Outline each blood parasite and name the species.
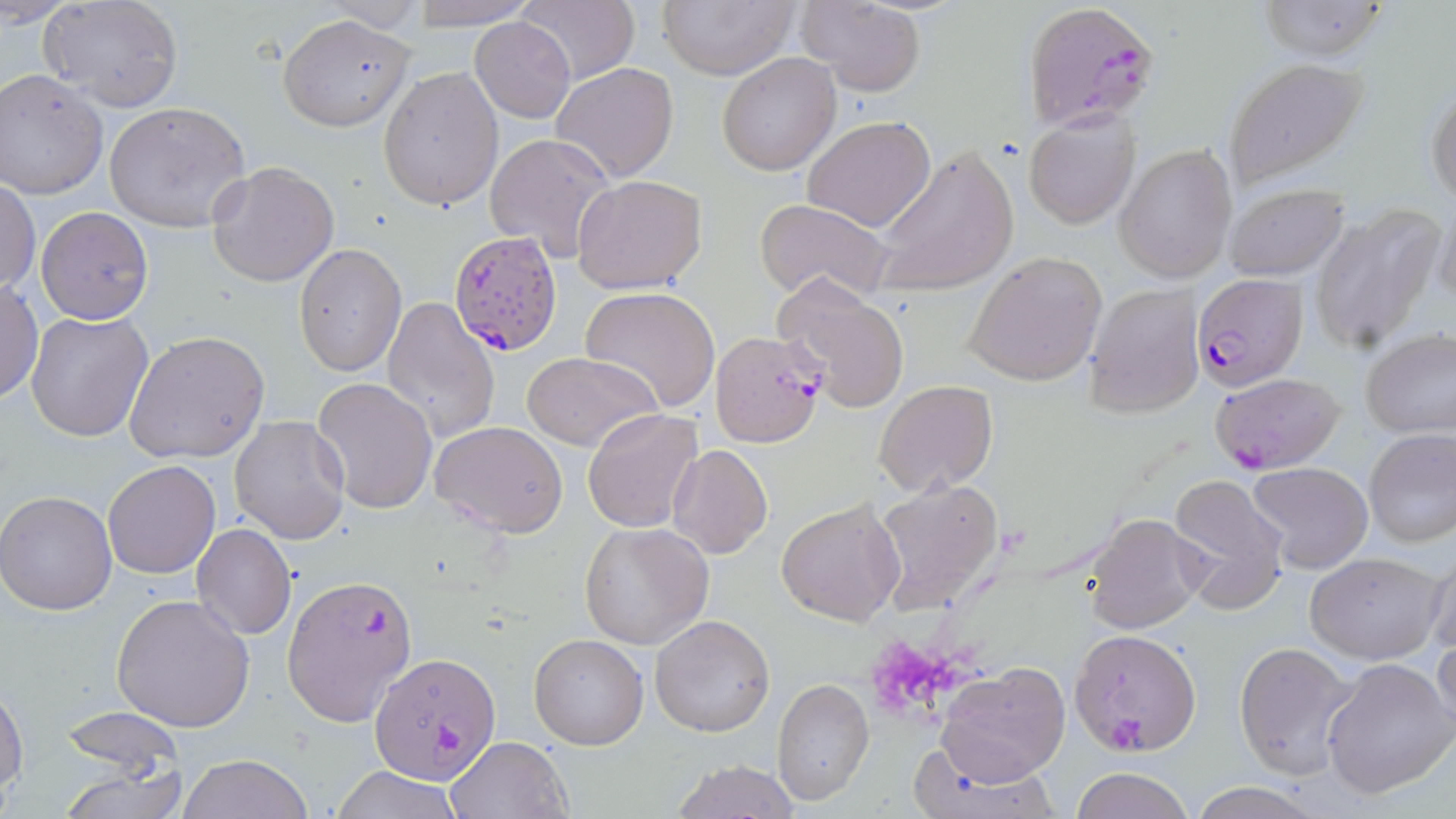

Approximate bounding boxes as (x1,y1)-(x2,y2) corner pairs in pixels.
Plasmodium falciparum-infected red blood cells: (1025,5)-(1161,138), (447,230)-(563,358), (1193,272)-(1307,390), (710,328)-(828,450), (1208,372)-(1347,475), (283,572)-(417,727), (1070,629)-(1202,754), (368,653)-(501,787).
No Plasmodium ovale, Plasmodium malariae, Plasmodium vivax, Babesia divergens, or Trypanosoma brucei observed.

Summary:
  - Uninfected red blood cell locations: (38,0)-(184,111), (405,0)-(534,27), (513,0)-(639,86), (657,0)-(802,79), (799,0)-(926,96), (1258,0)-(1392,61), (319,1)-(427,32), (279,14)-(415,132), (471,15)-(575,122), (716,54)-(840,175), (1224,57)-(1370,188), (550,62)-(679,183), (378,67)-(503,211), (0,70)-(108,200), (1427,85)-(1456,203), (104,100)-(253,233), (1023,110)-(1140,229), (802,116)-(935,234), (485,132)-(617,262), (870,144)-(1019,296), (1114,144)-(1236,283), (207,162)-(339,287), (574,174)-(709,293), (1,180)-(39,294), (1225,182)-(1350,281), (754,198)-(895,305), (1432,203)-(1456,309), (1308,204)-(1444,355), (37,206)-(153,324), (295,243)-(406,377), (963,252)-(1108,387), (773,276)-(910,414), (1,279)-(43,403), (1082,284)-(1203,419), (580,286)-(721,412), (382,297)-(502,443), (26,311)-(153,442), (1359,327)-(1456,439), (124,330)-(270,466), (522,351)-(660,451), (310,375)-(438,514), (875,379)-(999,495), (583,407)-(702,532), (229,414)-(351,545), (430,420)-(570,536), (1364,430)-(1456,548), (666,444)-(773,561), (103,460)-(219,578), (1246,461)-(1374,575), (1166,472)-(1289,615), (872,478)-(1005,612), (0,490)-(117,615), (776,498)-(904,627), (1085,513)-(1207,637), (578,522)-(715,649), (191,523)-(297,640), (1424,545)-(1456,665), (1304,550)-(1445,664), (110,593)-(257,733), (649,613)-(777,738), (1433,633)-(1456,743), (528,634)-(648,750), (1233,641)-(1364,780), (1321,657)-(1456,799), (939,661)-(1070,785), (773,678)-(874,805), (0,683)-(26,802), (59,705)-(184,781), (447,735)-(571,819), (902,741)-(1062,818), (177,754)-(315,819), (668,759)-(802,818), (58,762)-(188,819), (330,766)-(463,819), (1070,766)-(1193,819), (1185,783)-(1326,818)
  - Slide-level diagnosis: Plasmodium falciparum
  - Image size: 1456×819 pixels
  - Magnification: 1000x
  - Modality: light microscopy
  - Field of view: one of a larger specimen
  - Preparation: thin blood film
  - Stain: May-Grünwald-Giemsa